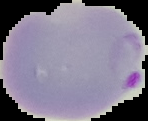

image_type: cell region segmented out of the field of view; surrounding area masked to black
image_size: 148×121 pixels
result: Plasmodium parasites detected
preparation: thin blood film